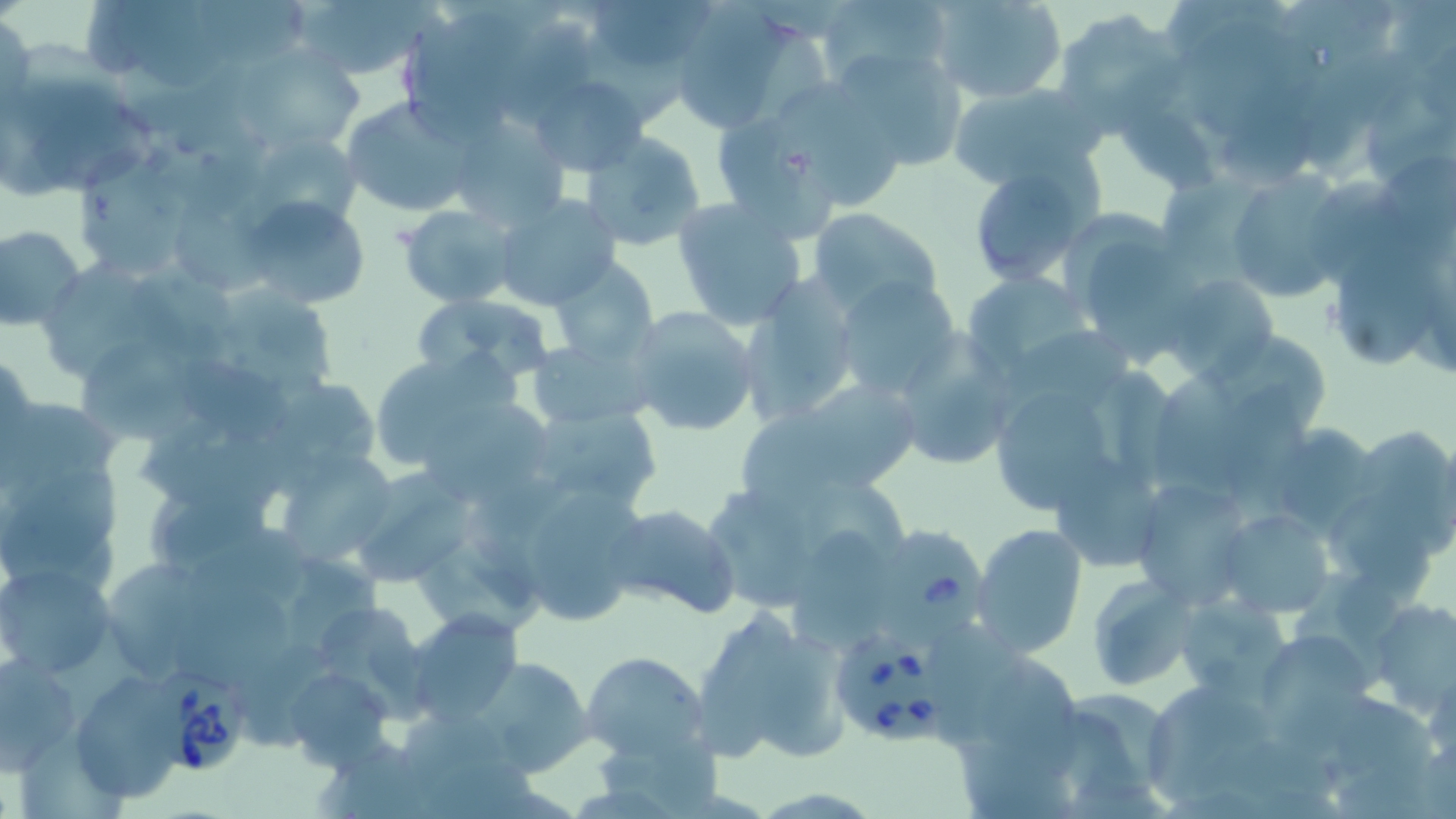
slide_level_diagnosis: Babesia divergens
field_of_view: single
preparation: thin blood smear
modality: light microscopy
uninfected_red_blood_cell_locations: 'approximate bounding boxes as [x1, y1, x2, y2] in pixels: [290, 0, 436, 82], [590, 0, 713, 62], [814, 0, 948, 91], [931, 0, 1069, 104], [112, 1, 230, 91], [195, 3, 307, 63], [666, 8, 803, 133], [1052, 9, 1184, 133], [1, 13, 35, 118], [1188, 21, 1305, 134], [236, 44, 368, 155], [831, 47, 971, 172], [3, 50, 157, 193], [527, 73, 650, 175], [946, 81, 1104, 189], [785, 84, 900, 202], [340, 97, 478, 218], [1120, 108, 1218, 195], [444, 114, 567, 231], [719, 125, 834, 242], [577, 130, 706, 252], [266, 135, 361, 219], [1373, 152, 1456, 252], [964, 155, 1102, 288], [81, 156, 196, 274], [1223, 170, 1353, 303], [1313, 175, 1404, 290], [492, 193, 622, 310], [240, 195, 372, 308], [671, 197, 809, 329], [177, 198, 271, 295], [399, 202, 520, 308], [807, 206, 947, 320], [1, 225, 85, 330], [1090, 241, 1188, 365], [1341, 243, 1442, 368], [548, 255, 659, 365], [49, 258, 161, 379], [132, 259, 238, 361], [958, 270, 1099, 382], [1162, 270, 1280, 383], [737, 276, 859, 423], [833, 276, 963, 401], [223, 291, 340, 386], [412, 292, 556, 388], [624, 305, 762, 437], [1005, 323, 1133, 422], [530, 338, 654, 431], [893, 338, 1018, 472], [80, 343, 199, 443], [364, 352, 524, 479], [187, 358, 289, 442], [1155, 365, 1243, 484], [780, 378, 926, 492], [1214, 380, 1313, 495], [991, 387, 1112, 514], [424, 395, 551, 499], [520, 401, 665, 515], [1266, 420, 1383, 536], [141, 431, 294, 514], [275, 450, 402, 570], [2, 451, 123, 593], [1052, 453, 1168, 568], [346, 468, 481, 590], [1128, 479, 1254, 608], [526, 491, 646, 625], [147, 493, 269, 559], [605, 503, 741, 619], [1219, 508, 1335, 617], [971, 523, 1088, 658], [189, 524, 311, 603], [793, 524, 885, 648], [421, 550, 542, 639], [111, 561, 213, 676], [0, 562, 118, 679], [1088, 575, 1197, 690], [166, 591, 295, 680], [1177, 595, 1290, 695], [312, 599, 426, 705], [1363, 599, 1456, 716], [693, 604, 850, 768], [404, 609, 523, 727], [1261, 635, 1377, 710], [583, 651, 710, 763], [0, 654, 81, 768], [469, 655, 593, 777], [975, 656, 1086, 782], [283, 667, 396, 770], [69, 673, 184, 804], [1146, 688, 1267, 805], [1064, 690, 1174, 798], [402, 711, 511, 803], [600, 739, 726, 811]'
magnification: 1000x
babesia_divergens_infected_red_blood_cell_locations: 'approximate bounding boxes as [x1, y1, x2, y2] in pixels: [870, 522, 991, 646], [833, 634, 953, 744], [149, 667, 250, 771]'
image_size: 1456×819 pixels
stain: May-Grünwald-Giemsa